Locate every uninfected red blood cell.
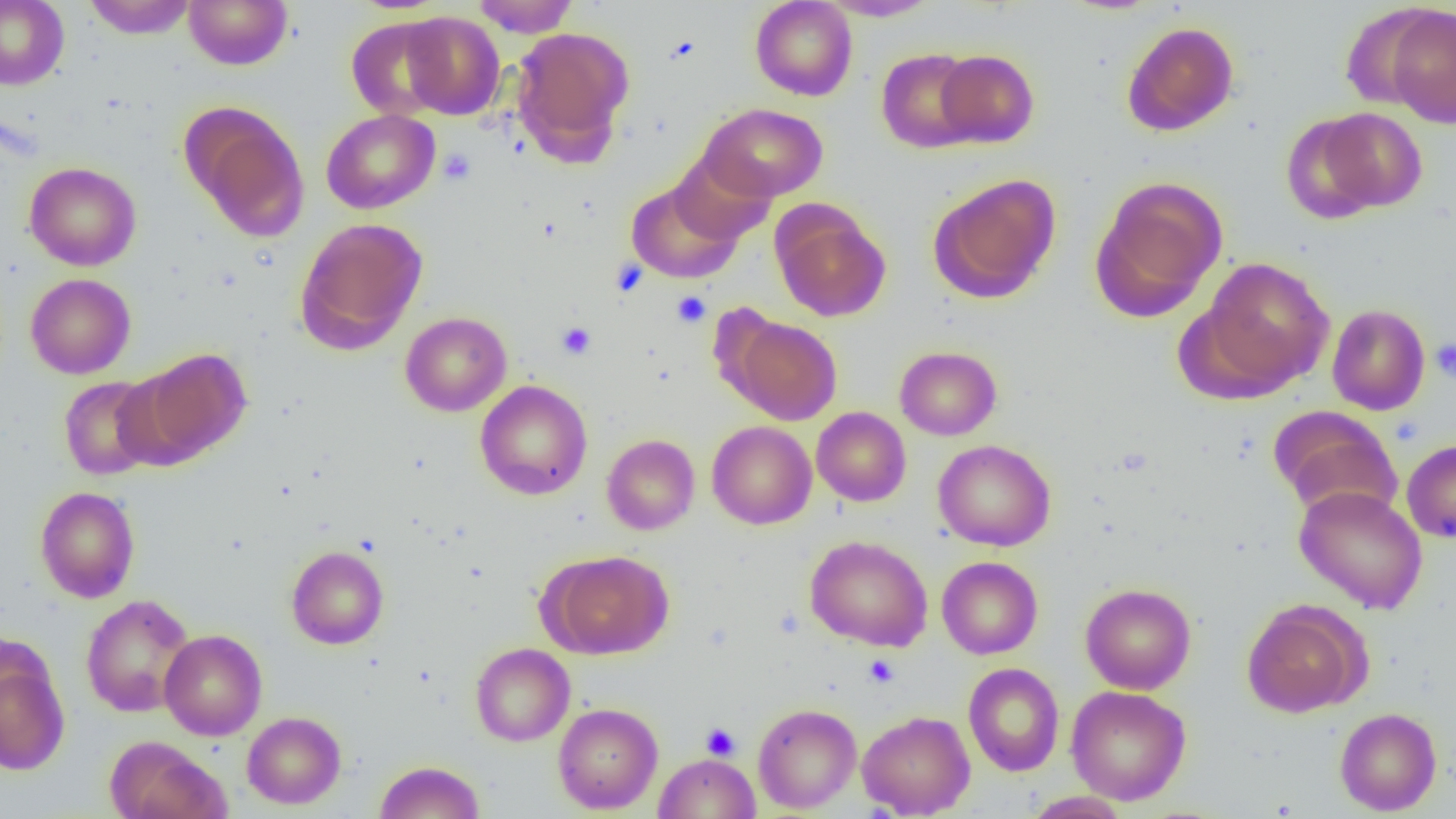

Approximate bounding boxes as named x1/y1/x2/y2 corners in pixels.
Uninfected red blood cells: (x1=0, y1=0, x2=69, y2=90), (x1=83, y1=0, x2=198, y2=39), (x1=183, y1=0, x2=293, y2=70), (x1=472, y1=0, x2=579, y2=37), (x1=750, y1=0, x2=858, y2=101), (x1=819, y1=0, x2=941, y2=21), (x1=1382, y1=5, x2=1456, y2=128), (x1=400, y1=11, x2=505, y2=120), (x1=346, y1=16, x2=452, y2=120), (x1=1121, y1=21, x2=1239, y2=136), (x1=510, y1=26, x2=634, y2=160), (x1=875, y1=48, x2=982, y2=153), (x1=935, y1=49, x2=1039, y2=148), (x1=181, y1=103, x2=310, y2=241), (x1=699, y1=103, x2=828, y2=202), (x1=1313, y1=107, x2=1427, y2=213), (x1=321, y1=109, x2=440, y2=214), (x1=1281, y1=113, x2=1388, y2=225), (x1=668, y1=150, x2=775, y2=246), (x1=24, y1=162, x2=141, y2=271), (x1=927, y1=173, x2=1062, y2=304), (x1=1089, y1=176, x2=1228, y2=321), (x1=626, y1=178, x2=744, y2=283), (x1=771, y1=202, x2=890, y2=322), (x1=294, y1=217, x2=428, y2=354), (x1=1198, y1=256, x2=1335, y2=394), (x1=25, y1=273, x2=136, y2=379), (x1=1327, y1=304, x2=1430, y2=415), (x1=400, y1=311, x2=512, y2=416), (x1=729, y1=317, x2=842, y2=425), (x1=894, y1=346, x2=1002, y2=441), (x1=135, y1=348, x2=253, y2=461), (x1=58, y1=376, x2=163, y2=481), (x1=475, y1=380, x2=592, y2=500), (x1=811, y1=407, x2=911, y2=506), (x1=1270, y1=407, x2=1402, y2=519), (x1=707, y1=421, x2=817, y2=529), (x1=602, y1=434, x2=700, y2=535), (x1=933, y1=439, x2=1057, y2=552), (x1=1402, y1=439, x2=1456, y2=543), (x1=1294, y1=485, x2=1428, y2=614), (x1=34, y1=486, x2=141, y2=603), (x1=805, y1=535, x2=933, y2=651), (x1=286, y1=545, x2=389, y2=649), (x1=542, y1=550, x2=672, y2=659), (x1=936, y1=556, x2=1043, y2=659), (x1=1080, y1=583, x2=1196, y2=694), (x1=80, y1=594, x2=195, y2=717), (x1=1241, y1=600, x2=1368, y2=717), (x1=159, y1=629, x2=267, y2=740), (x1=470, y1=643, x2=575, y2=746), (x1=0, y1=655, x2=70, y2=776), (x1=963, y1=663, x2=1065, y2=776), (x1=1066, y1=685, x2=1192, y2=805), (x1=553, y1=703, x2=663, y2=814), (x1=753, y1=703, x2=862, y2=813), (x1=1334, y1=707, x2=1442, y2=815), (x1=857, y1=710, x2=975, y2=818), (x1=242, y1=711, x2=346, y2=809), (x1=104, y1=735, x2=230, y2=819), (x1=655, y1=753, x2=760, y2=818), (x1=374, y1=760, x2=485, y2=819), (x1=1023, y1=791, x2=1131, y2=818).

Summary:
  - Platelet locations: (x1=438, y1=148, x2=476, y2=184), (x1=611, y1=259, x2=648, y2=297), (x1=672, y1=291, x2=711, y2=327), (x1=557, y1=322, x2=596, y2=359), (x1=1430, y1=338, x2=1456, y2=382), (x1=863, y1=654, x2=899, y2=686), (x1=700, y1=723, x2=741, y2=760)
  - Slide-level diagnosis: no evidence of blood parasites
  - Modality: optical microscopy
  - Field of view: one of a larger specimen
  - Preparation: thin blood film
  - Magnification: 1000x
  - Image size: 1456×819 pixels